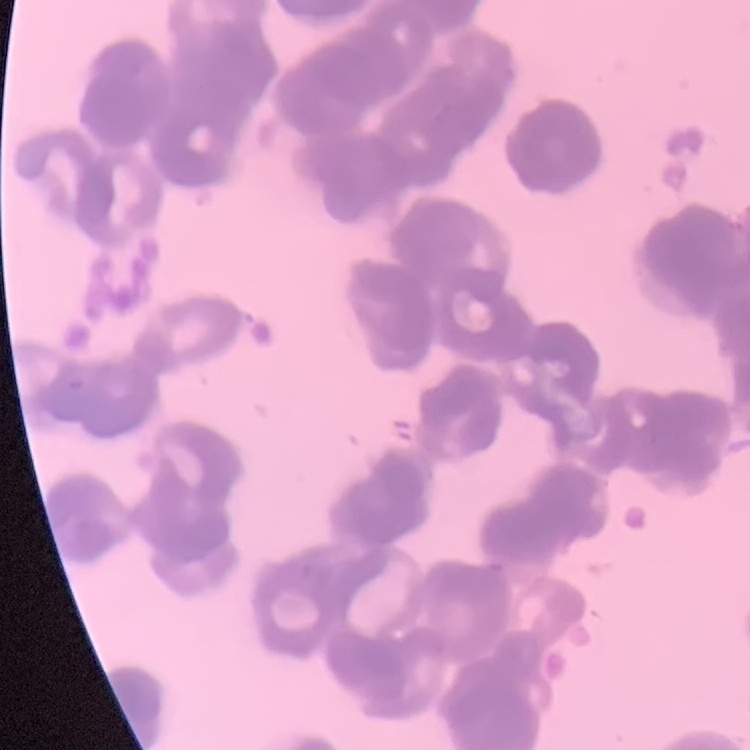
Summary:
  - Red blood cell morphology: rouleaux formation
  - Image type: square crop of a larger photomicrograph
  - Preparation: thin blood film
  - Stain: Field's or Giemsa